Name the parasite shown.
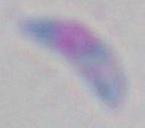

This is Toxoplasma gondii.

Summary:
  - Magnification: 1000x
  - Modality: micrograph